State which parasite is depicted.
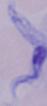

A trypanosome.

Summary:
  - Modality: photomicrograph
  - Magnification: 1000x